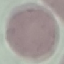

result: negative for malaria parasites
preparation: thin smear
capture: smartphone camera at the microscope eyepiece
stain: Giemsa
image_type: cell patch, automatically extracted from a larger field of view and resized to 64 × 64 pixels